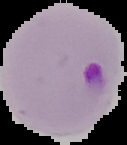
Summary:
  - Malaria status: parasitized
  - Image size: 127×145 pixels
  - Image type: segmented cell region with the area outside set to black
  - Preparation: thin blood film